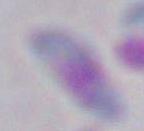
identification = Toxoplasma gondii
magnification = 1000x
modality = micrograph